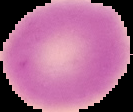 From a thin blood film. Image is 133×112 pixels. Result: no Plasmodium parasites seen. Segmented cell region on a black background.